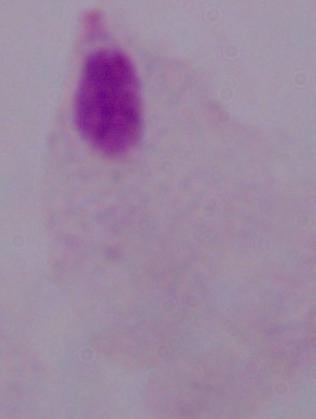
magnification = 1000x
modality = photomicrograph
identification = trichomonad